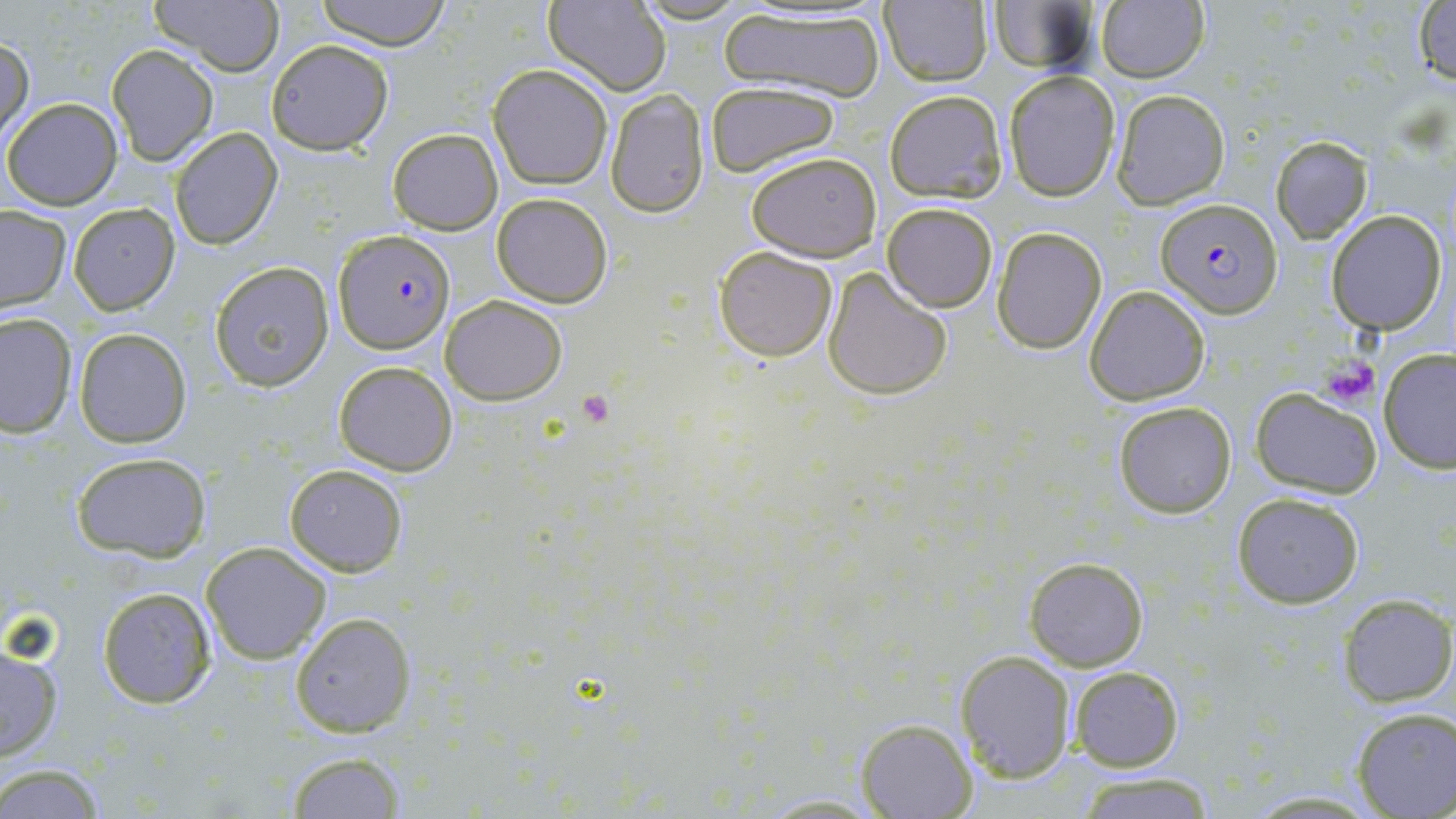
{
  "slide_level_diagnosis": "Plasmodium falciparum",
  "platelet_locations": "approximate bounding boxes as [x1, y1, x2, y2] in pixels: [1319, 353, 1380, 407], [576, 388, 616, 427]",
  "plasmodium_falciparum_infected_red_blood_cell_locations": "approximate bounding boxes as [x1, y1, x2, y2] in pixels: [1158, 196, 1284, 317], [332, 229, 456, 353]",
  "preparation": "thin blood smear",
  "uninfected_red_blood_cell_locations": "approximate bounding boxes as [x1, y1, x2, y2] in pixels: [151, 0, 281, 75], [315, 0, 451, 48], [543, 0, 672, 94], [634, 1, 748, 24], [879, 1, 993, 88], [985, 3, 1099, 76], [1096, 3, 1209, 82], [1412, 3, 1455, 88], [719, 6, 887, 100], [0, 34, 33, 147], [265, 39, 393, 155], [106, 45, 218, 166], [487, 64, 613, 189], [1003, 71, 1121, 201], [704, 80, 841, 178], [603, 88, 711, 218], [884, 90, 1008, 203], [1110, 90, 1230, 208], [2, 98, 123, 209], [169, 127, 282, 250], [387, 128, 503, 235], [1271, 136, 1374, 243], [745, 151, 882, 262], [491, 192, 612, 308], [67, 202, 180, 315], [880, 204, 998, 313], [0, 205, 71, 312], [1326, 210, 1447, 334], [991, 227, 1107, 354], [714, 246, 837, 363], [208, 262, 335, 391], [822, 266, 952, 401], [1085, 285, 1210, 404], [440, 295, 567, 404], [0, 311, 77, 437], [73, 327, 190, 447], [1379, 352, 1456, 475], [334, 361, 458, 476], [1251, 387, 1382, 497], [1112, 399, 1237, 519], [69, 451, 212, 562], [284, 463, 408, 575], [1231, 492, 1365, 607], [200, 541, 332, 664], [1024, 556, 1149, 670], [96, 585, 216, 709], [1336, 594, 1455, 708], [289, 612, 415, 737], [0, 643, 64, 760], [955, 650, 1076, 781], [1067, 666, 1183, 771], [1351, 709, 1456, 818], [857, 718, 976, 817], [285, 750, 409, 819], [0, 764, 107, 819], [1071, 772, 1220, 818], [1238, 790, 1385, 817], [749, 792, 889, 817]",
  "stain": "May-Grünwald-Giemsa",
  "modality": "light microscopy",
  "field_of_view": "single",
  "magnification": "1000x",
  "image_size": "1456×819 pixels"
}